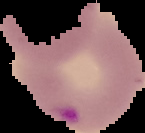

image_size: 145×133 pixels
result: Plasmodium parasites detected
preparation: thin blood smear
image_type: cell region segmented out of the field of view; surrounding area masked to black